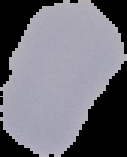

image type = segmented cell region with the area outside set to black
image size = 127×157 pixels
preparation = thin blood film
result = no malaria parasites detected